Give the preparation type.
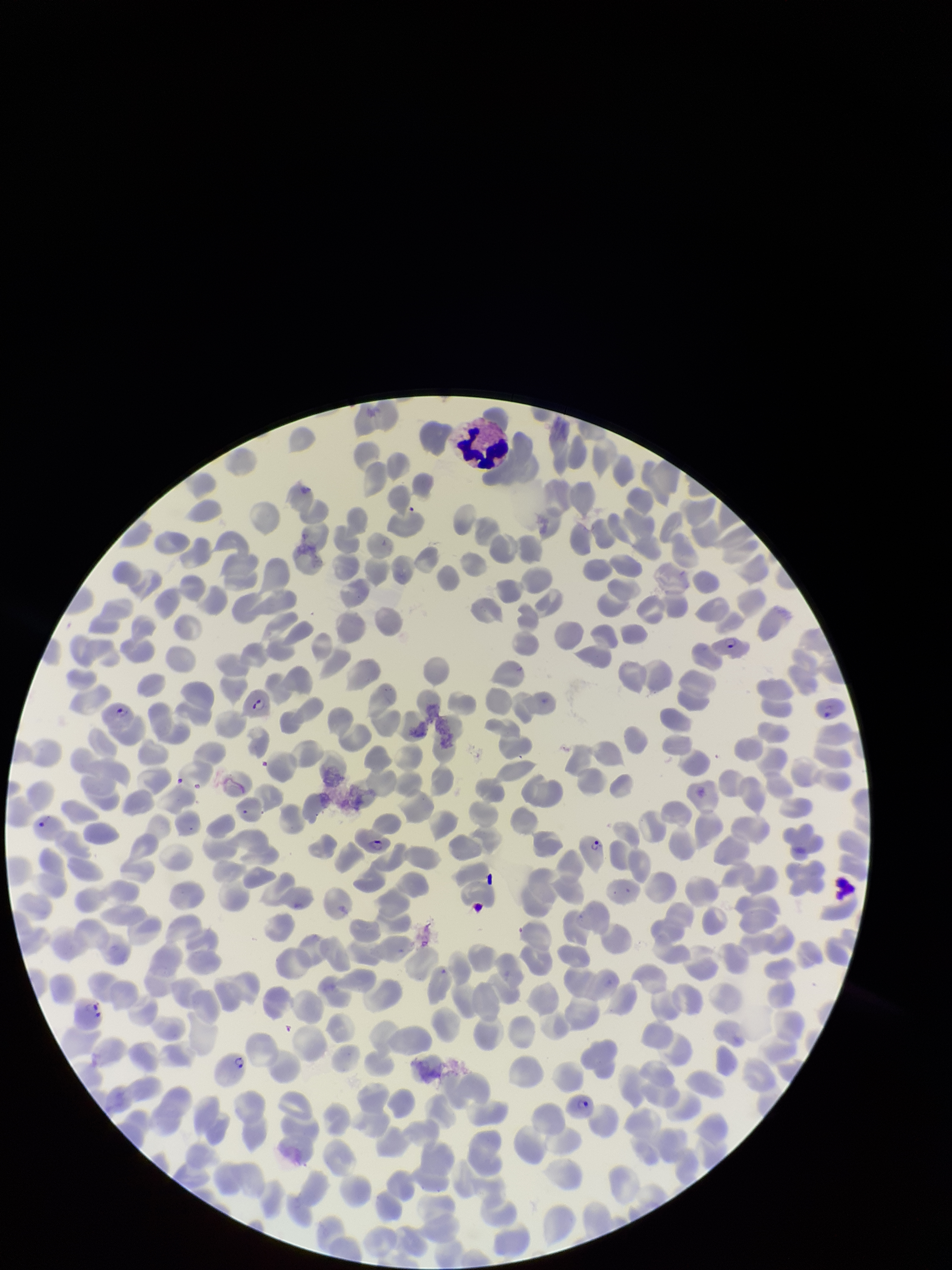
Thin.

Summary:
  - Stain: Giemsa
  - Patient malaria status: positive
  - Field of view: single
  - Parasitized red blood cell count: 9
  - Red blood cell count: 367
  - Capture: smartphone photograph through the microscope eyepiece
  - Parasitized red blood cells: seen
  - Image size: 952×1270 pixels
  - Species reported for this patient: Plasmodium falciparum